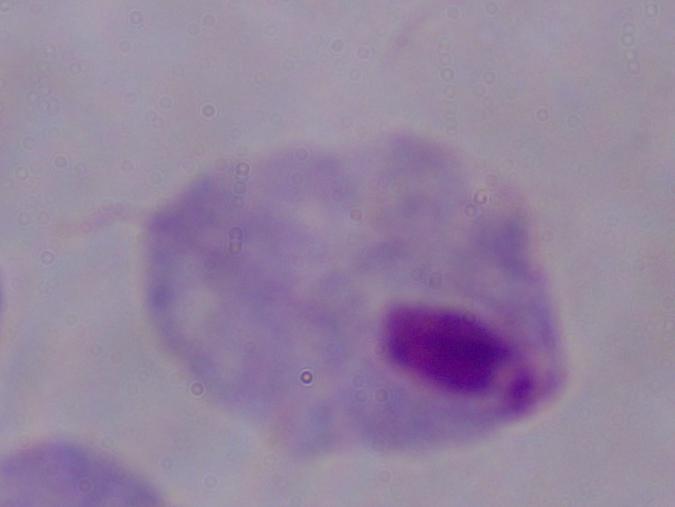

Micrograph. A trichomonad is shown. 1000x magnification.